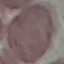

Malaria status: uninfected. Giemsa stain. Cell patch, automatically extracted from a larger field of view and resized to 64 × 64 pixels. Photographed with a smartphone camera at the microscope eyepiece. Thin smear of blood.